Comment on the morphology of the red blood cells.
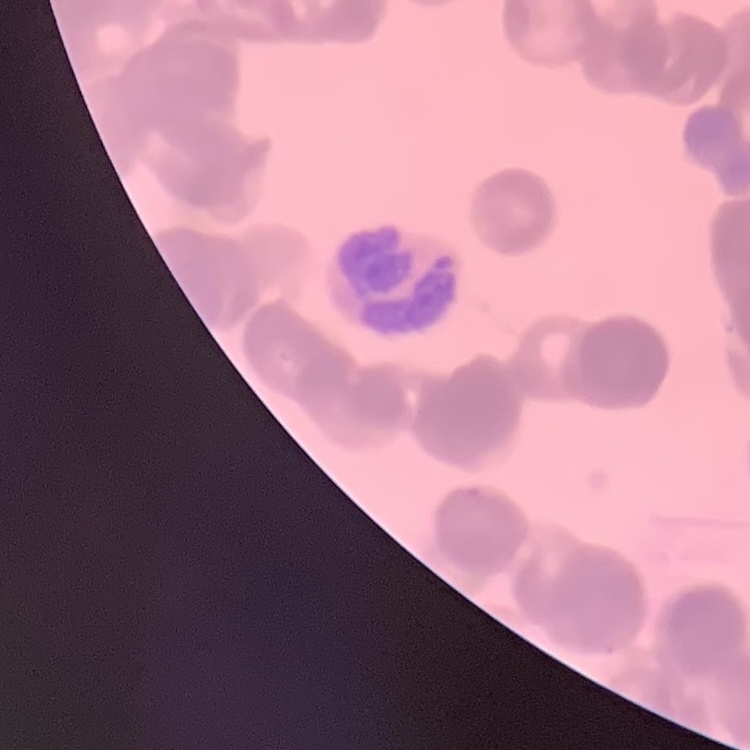
Rouleaux formation.

Thin peripheral smear. Stained with either Field's or Giemsa. Square crop of a larger photomicrograph.